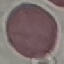

{
  "result": "no malaria parasites seen",
  "stain": "Giemsa",
  "capture": "smartphone through the microscope eyepiece",
  "preparation": "thin blood smear",
  "image_type": "automatically extracted cell patch, resized to 64 × 64 pixels"
}